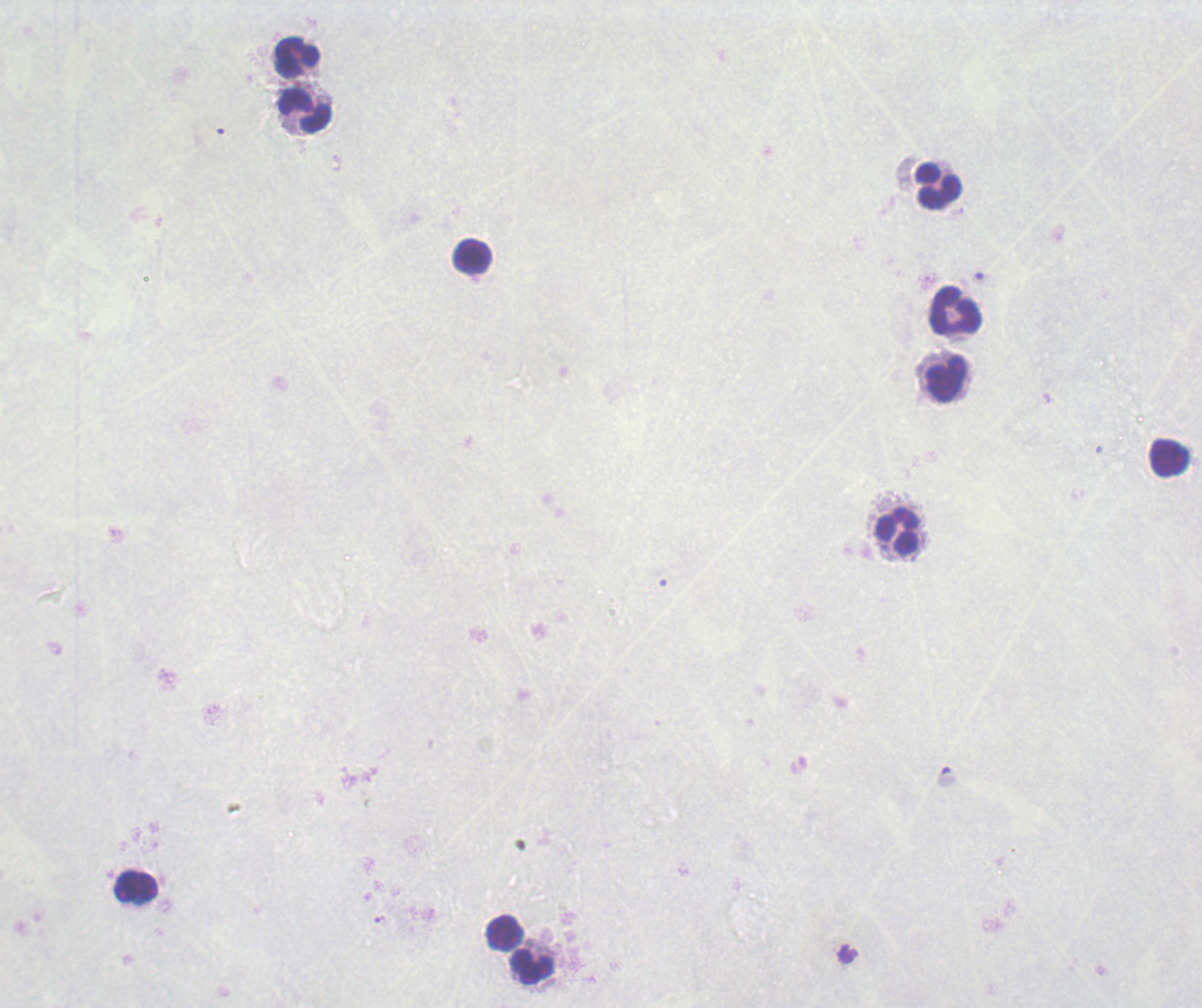
stain: Romanowsky
preparation: thick blood smear
background_quality: poor
field_of_view: one from this slide
context: previously used in an actual diagnosis
magnification: 100x
image_size: 1202×1008 pixels
leukocyte_locations: 'approximate centers as {x, y} in pixels: {297, 59}, {305, 112}, {939, 186}, {473, 258}, {955, 311}, {946, 379}, {1169, 457}, {898, 532}, {136, 887}, {504, 933}, {533, 967}'
result: no Plasmodium parasites seen